Look for Plasmodium parasites.
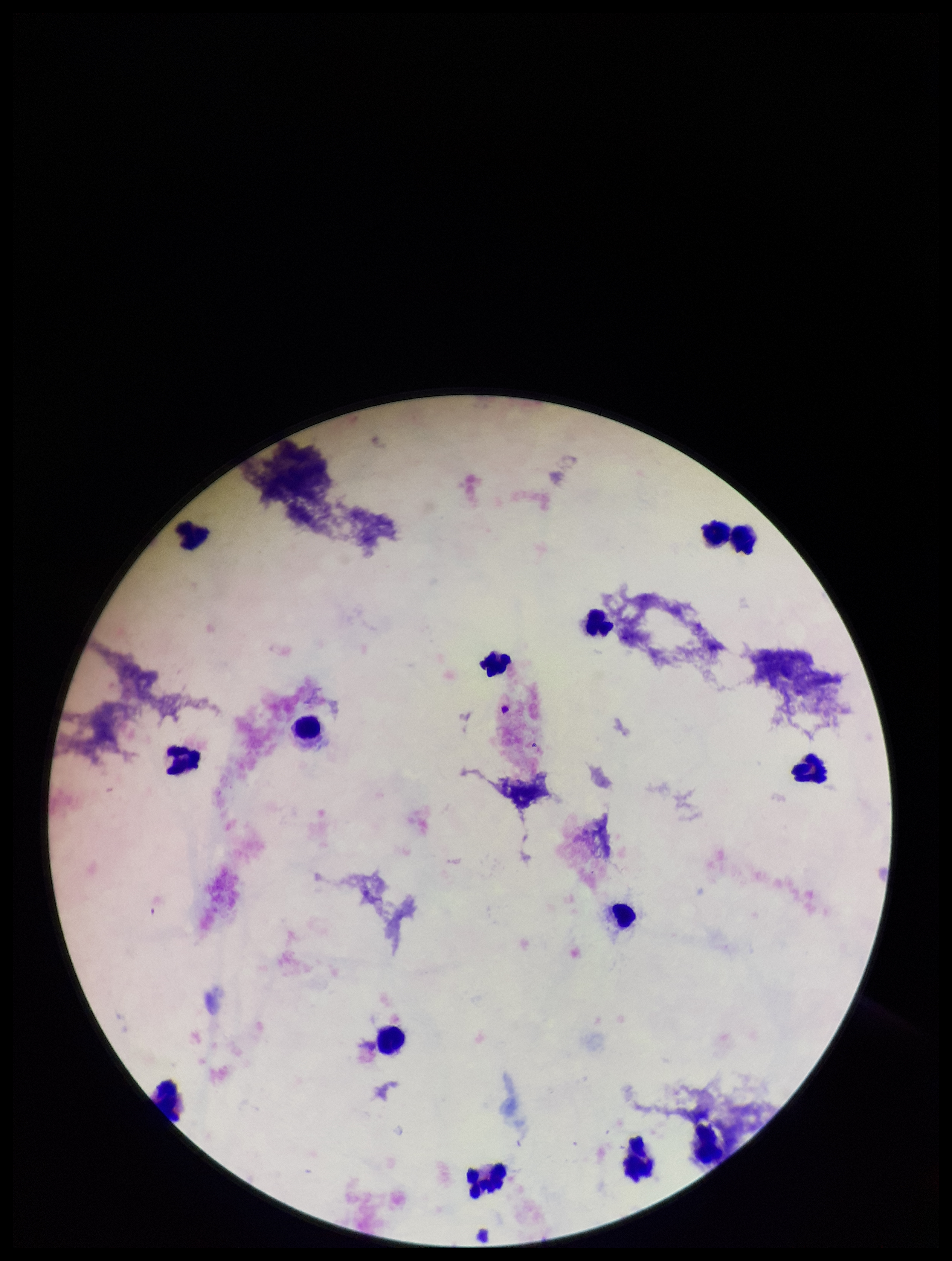
None identified.

leukocyte_count: 14
capture: smartphone photograph through the microscope eyepiece
patient_malaria_status: negative
preparation: thick smear
field_of_view: one from this slide
parasite_count: 0
stain: Giemsa
image_size: 952×1261 pixels